Report the malaria status of this cell.
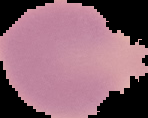

It is uninfected.

Summary:
  - Image type: segmented cell region with the area outside set to black
  - Preparation: thin blood smear
  - Image size: 148×118 pixels